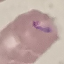
Result: malaria parasites detected. Giemsa-stained preparation. Cell patch, automatically extracted from a larger field of view and resized to 64 × 64 pixels. Thin smear of blood. Acquired by smartphone through the microscope eyepiece.